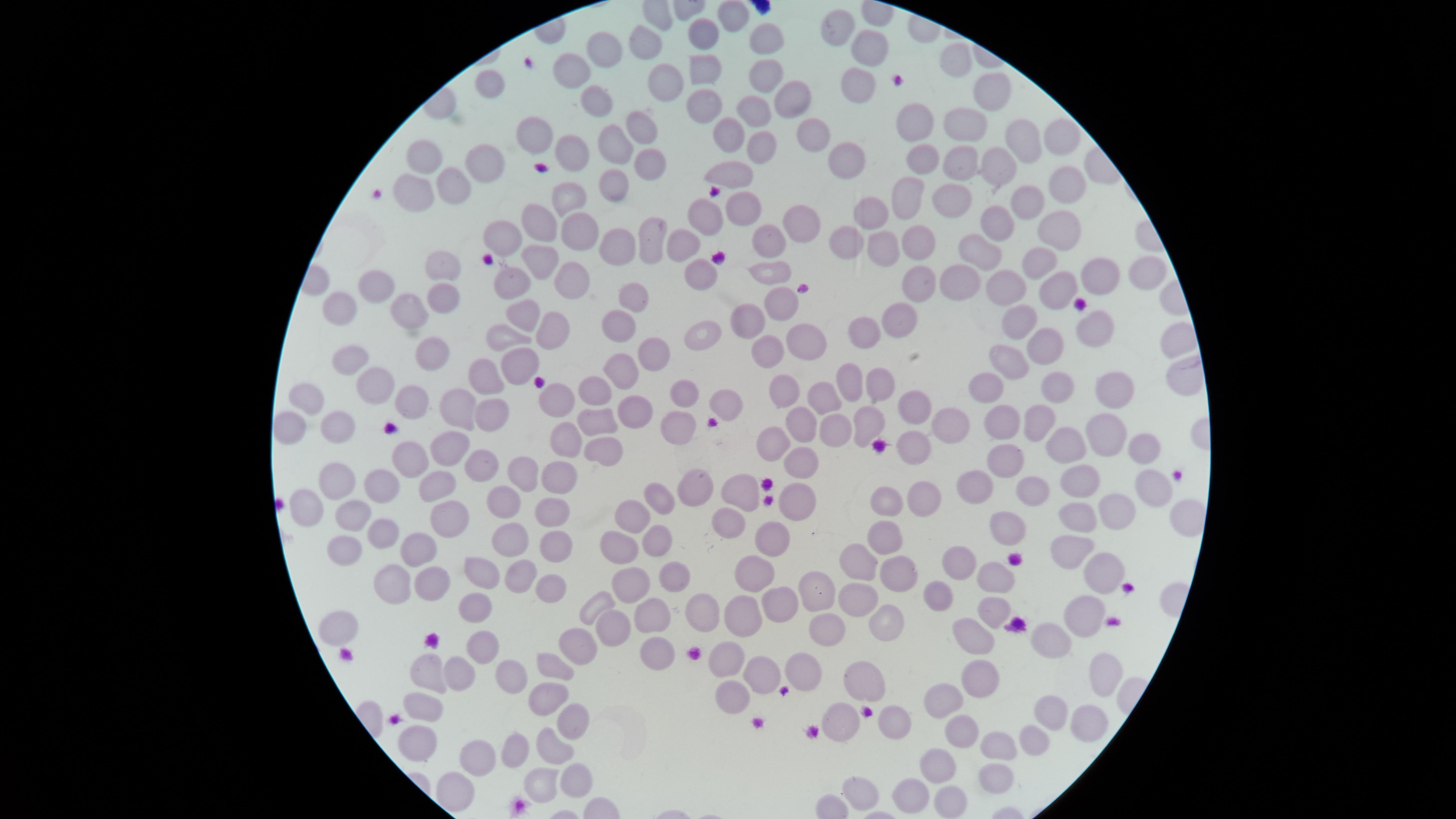
presence = no malaria parasites detected
uninfected red blood cells = approximate marker points as {x, y} in pixels: {730, 15}, {839, 22}, {765, 35}, {700, 39}, {869, 43}, {648, 44}, {605, 47}, {956, 57}, {575, 69}, {703, 69}, {764, 71}, {494, 78}, {857, 89}, {664, 90}, {602, 93}, {995, 97}, {788, 98}, {704, 105}, {750, 113}, {968, 117}, {918, 122}, {641, 123}, {543, 131}, {726, 133}, {812, 135}, {1016, 135}, {1064, 139}, {616, 147}, {756, 147}, {579, 150}, {429, 159}, {488, 159}, {928, 161}, {650, 162}, {965, 165}, {847, 167}, {996, 169}, {734, 172}, {455, 180}, {1070, 182}, {615, 187}, {420, 188}, {566, 193}, {907, 198}, {956, 198}, {1022, 200}, {745, 203}, {868, 213}, {708, 214}, {536, 216}, {999, 217}, {797, 225}, {1061, 225}, {578, 227}, {509, 234}, {912, 236}, {653, 237}, {848, 239}, {683, 243}, {768, 244}, {883, 245}, {623, 247}, {974, 250}, {1044, 256}, {547, 257}, {440, 267}, {700, 270}, {768, 272}, {917, 273}, {1137, 275}, {953, 277}, {576, 280}, {506, 281}, {1089, 282}, {1050, 283}, {1013, 284}, {371, 285}, {439, 298}, {631, 298}, {782, 302}, {341, 310}, {406, 312}, {518, 313}, {908, 316}, {1026, 321}, {620, 322}, {757, 322}, {551, 330}, {710, 332}, {860, 332}, {1095, 332}, {508, 339}, {1041, 344}, {806, 346}, {770, 348}, {351, 352}, {646, 356}, {432, 359}, {1010, 361}, {519, 366}, {622, 372}, {484, 377}, {378, 381}, {853, 382}, {987, 382}, {1058, 384}, {880, 385}, {1108, 386}, {688, 388}, {782, 389}, {598, 390}, {412, 395}, {306, 398}, {824, 398}, {722, 399}, {557, 401}, {911, 408}, {450, 409}, {999, 411}, {493, 412}, {633, 415}, {678, 417}, {1036, 420}, {795, 421}, {869, 423}, {831, 424}, {302, 425}, {344, 425}, {597, 427}, {944, 427}, {1110, 432}, {560, 439}, {1069, 441}, {1139, 442}, {773, 444}, {913, 445}, {452, 446}, {604, 452}, {419, 453}, {806, 458}, {1004, 458}, {489, 462}, {524, 470}, {557, 476}, {1086, 476}, {340, 479}, {977, 479}, {386, 482}, {434, 482}, {1033, 484}, {743, 485}, {1150, 485}, {698, 486}, {499, 493}, {662, 495}, {928, 496}, {889, 497}, {799, 498}, {309, 503}, {1117, 510}, {441, 511}, {550, 513}, {637, 514}, {348, 517}, {1076, 519}, {731, 520}, {1005, 528}, {382, 531}, {884, 532}, {773, 536}, {620, 538}, {656, 540}, {514, 542}, {553, 542}, {339, 547}, {414, 548}, {1061, 554}, {863, 560}, {962, 563}, {487, 572}, {758, 572}, {518, 575}, {897, 576}, {1098, 576}, {993, 577}, {671, 579}, {392, 580}, {547, 581}, {425, 582}, {811, 584}, {634, 586}, {936, 590}, {854, 596}, {597, 602}, {477, 604}, {709, 605}, {782, 605}, {998, 608}, {738, 614}, {650, 615}, {1087, 617}, {612, 624}, {340, 626}, {824, 626}, {884, 626}, {974, 636}, {1052, 638}, {582, 640}, {481, 644}, {652, 649}, {728, 656}, {560, 662}, {430, 668}, {806, 668}, {981, 670}, {757, 671}, {457, 674}, {505, 674}, {1100, 678}, {859, 682}, {946, 692}, {730, 694}, {546, 696}, {425, 706}, {1053, 709}, {841, 716}, {1087, 717}, {573, 720}, {893, 725}, {959, 726}, {1035, 738}, {416, 740}, {555, 745}, {993, 745}, {518, 751}, {487, 753}, {936, 761}, {997, 769}, {549, 783}, {453, 786}, {572, 786}, {857, 790}, {910, 797}, {942, 800}
field of view = single
stain = Giemsa
image size = 1456×819 pixels
visible region = circular
preparation = thin blood film
capture = smartphone photograph through the microscope eyepiece